Evaluate for Plasmodium parasites.
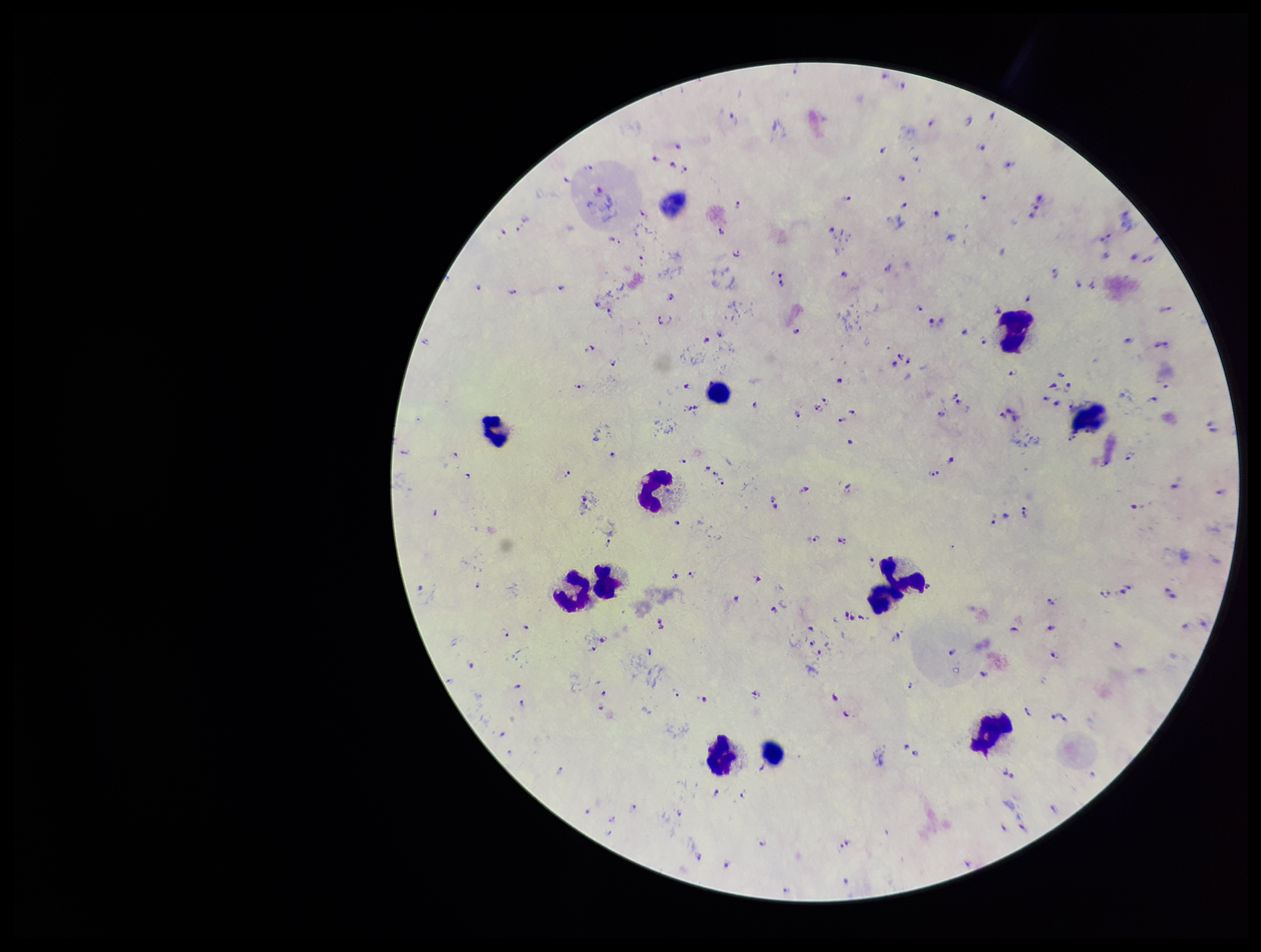
Detected.

Patient malaria status: positive. Single field of view. Preparation: thick smear. Species reported for this patient: Plasmodium falciparum. Image is 1261×952 pixels. Stained with Giemsa. Parasite count: 173. Photographed through the microscope eyepiece with a smartphone camera. Leukocyte count: 11.